Locate every uninfected red blood cell.
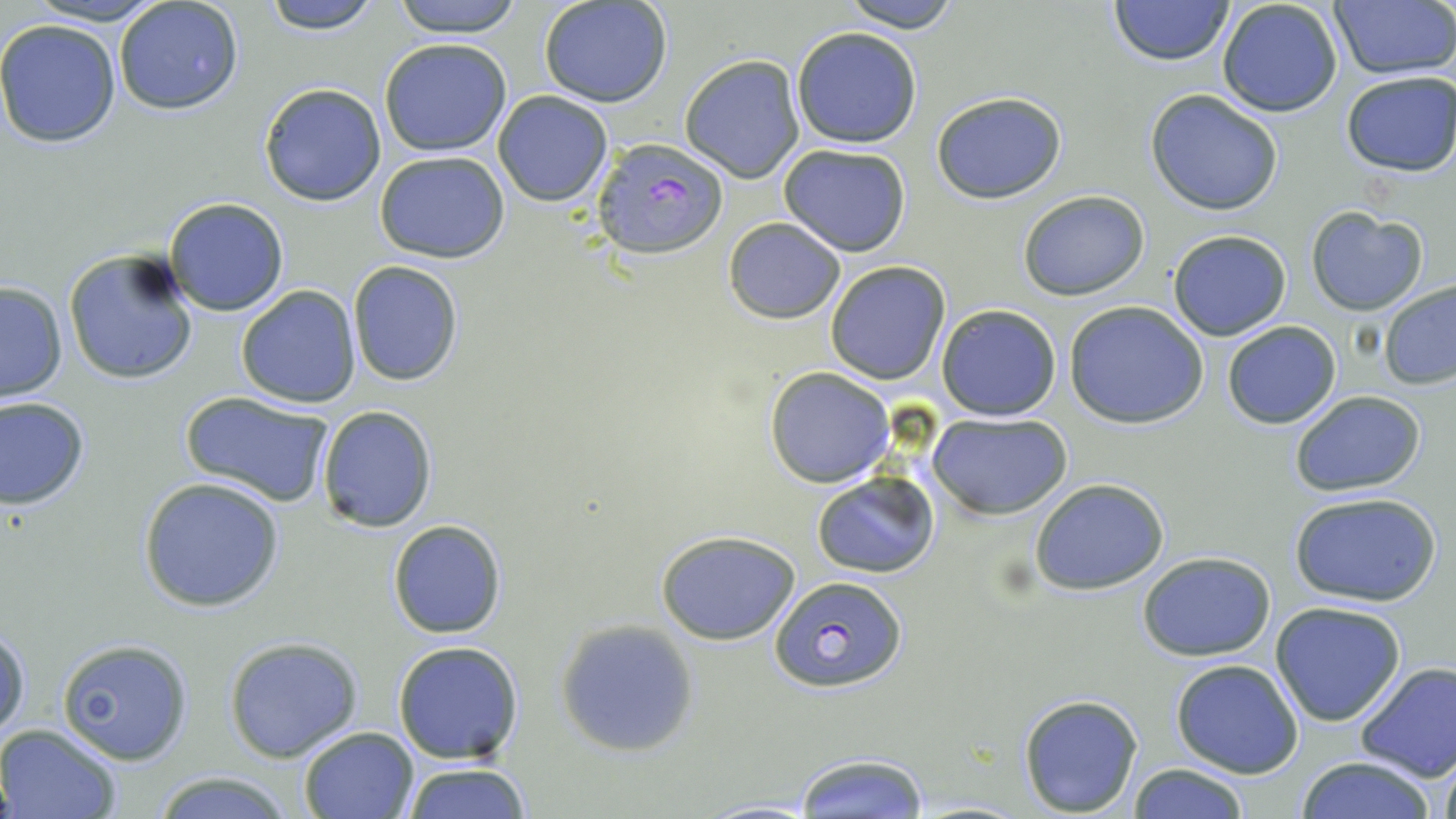

Approximate bounding boxes as (x1, y1, x2, y2) in pixels.
Uninfected red blood cells: (22, 0, 170, 25), (112, 0, 245, 116), (260, 0, 386, 33), (389, 0, 526, 37), (538, 0, 673, 107), (839, 0, 964, 31), (1107, 0, 1235, 67), (1329, 0, 1456, 79), (1216, 1, 1345, 118), (0, 18, 122, 148), (791, 26, 922, 148), (378, 38, 512, 155), (679, 54, 807, 183), (1340, 71, 1455, 176), (258, 82, 387, 206), (1146, 89, 1283, 215), (493, 91, 613, 206), (932, 92, 1067, 204), (778, 144, 913, 256), (374, 150, 512, 262), (1018, 190, 1150, 300), (164, 197, 290, 317), (1304, 207, 1429, 316), (723, 218, 847, 324), (1167, 230, 1292, 341), (63, 247, 199, 386), (347, 261, 464, 387), (824, 261, 951, 385), (1378, 280, 1456, 392), (0, 281, 68, 403), (235, 285, 362, 408), (1063, 300, 1210, 429), (937, 304, 1061, 420), (1221, 320, 1341, 429), (764, 366, 895, 486), (1287, 390, 1428, 495), (180, 391, 335, 507), (0, 395, 91, 510), (315, 405, 438, 531), (928, 412, 1072, 520), (811, 470, 940, 579), (137, 476, 285, 613), (1028, 478, 1171, 593), (1288, 492, 1444, 607), (387, 519, 506, 638), (656, 529, 800, 646), (1137, 552, 1278, 659), (1270, 600, 1407, 727), (556, 620, 698, 756), (0, 624, 30, 744), (222, 635, 363, 763), (56, 636, 195, 763), (392, 640, 525, 764), (1171, 659, 1303, 778), (1355, 661, 1456, 782), (1018, 692, 1145, 816), (1, 724, 121, 818), (297, 726, 419, 818), (792, 752, 929, 817), (1433, 752, 1456, 819), (1294, 755, 1440, 819), (401, 763, 533, 818), (1126, 763, 1252, 818), (151, 770, 296, 819), (693, 799, 827, 818).

slide-level diagnosis = Plasmodium falciparum
preparation = thin blood smear
image size = 1456×819 pixels
stain = May-Grünwald-Giemsa
modality = optical microscopy
field of view = single
magnification = 1000x
Plasmodium falciparum-infected red blood cell locations = approximate bounding boxes as (x1, y1, x2, y2) in pixels: (593, 138, 729, 262), (769, 574, 906, 695)